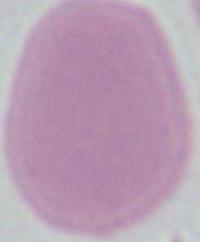
magnification: 1000x
identification: erythrocyte
modality: photomicrograph